Classify this cell by malaria status.
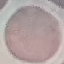

It is uninfected.

Giemsa stain. Thin blood smear. Automatically extracted cell patch, resized to 64 × 64 pixels. Photographed with a smartphone camera at the microscope eyepiece.